Give the preparation type.
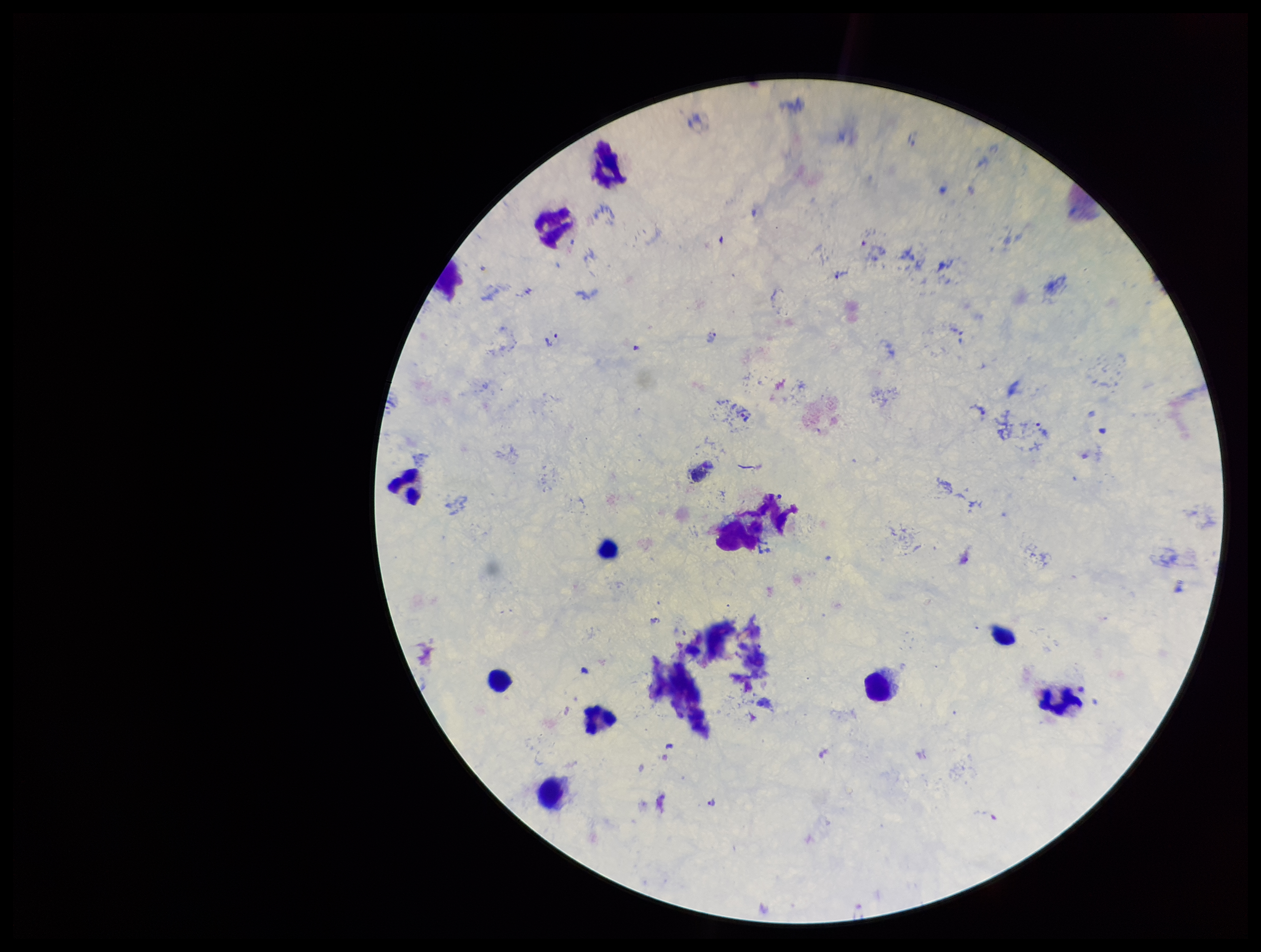

A thick smear.

Stained with Giemsa. Image is 1261×952 pixels. Photographed through the microscope eyepiece with a smartphone camera. Species reported for this patient: Plasmodium vivax. Patient malaria status: infected. Parasite count: 3. Plasmodium parasites: identified. Single field of view. Leukocyte count: 8.